Classify this cell by malaria status.
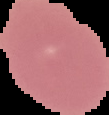
It is uninfected.

Summary:
  - Preparation: thin blood smear
  - Image size: 109×115 pixels
  - Image type: segmented cell region on a black background